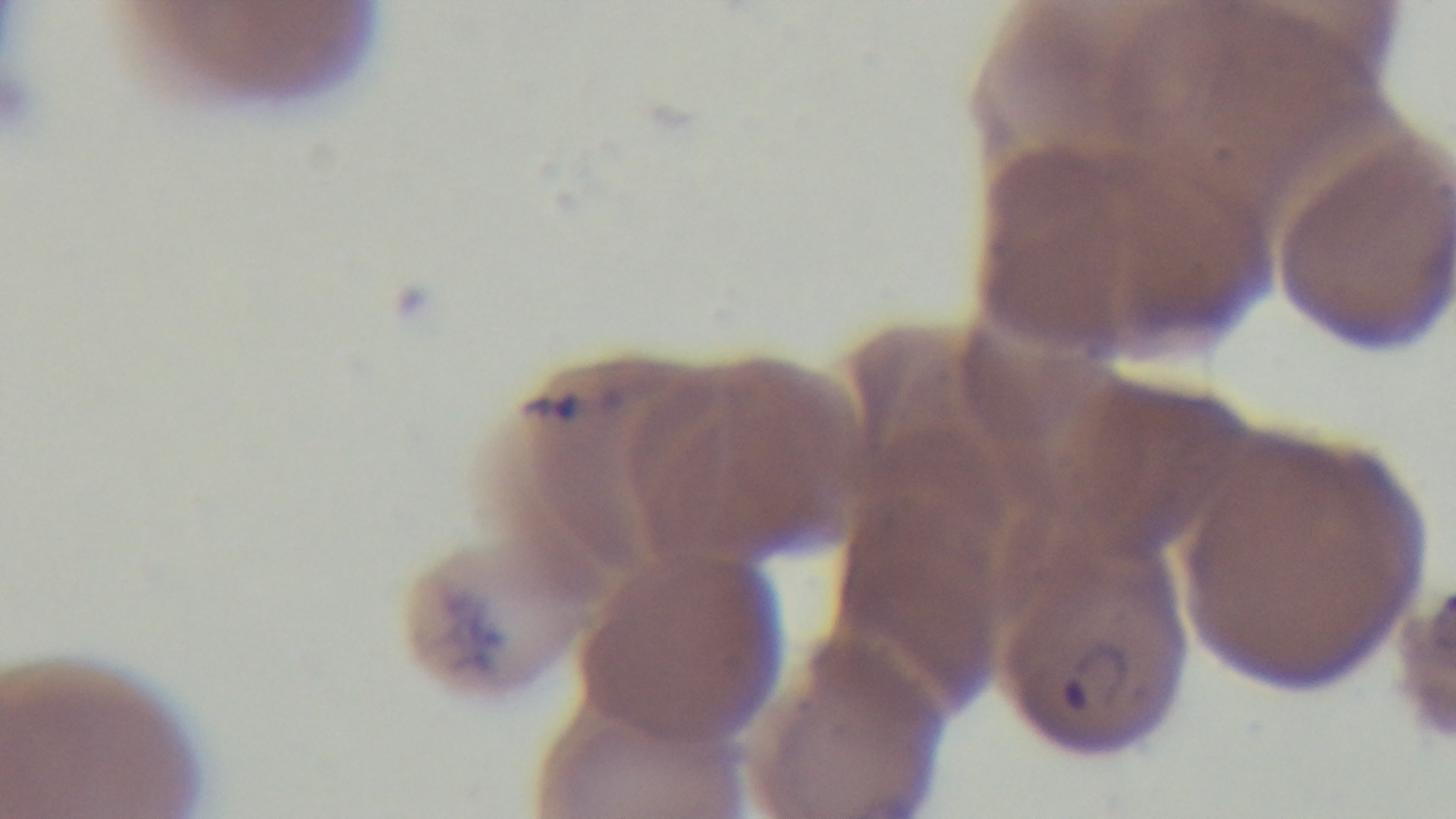

field of view = single
malaria status = infected
capture = mounted 4K digital camera
objective = 100x oil immersion
modality = light microscopy
preparation = thin smear
stain = Giemsa